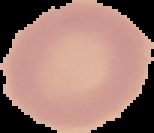
Summary:
  - Preparation: thin blood smear
  - Image type: cell region segmented out of the field of view; surrounding area masked to black
  - Malaria status: uninfected
  - Image size: 154×133 pixels